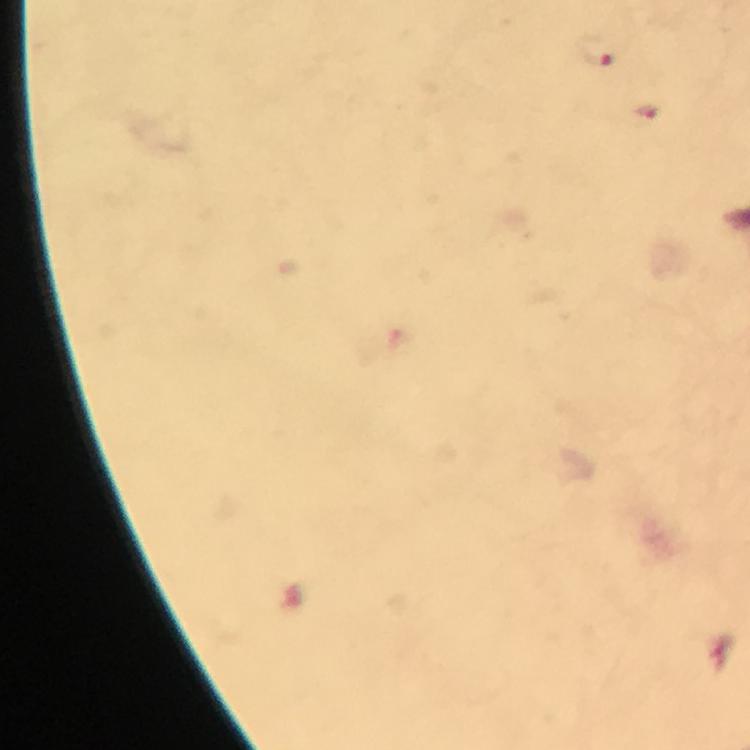

preparation = thick smear
image size = 750×750 pixels
immersion oil = used
capture = smartphone mounted on the microscope
magnification = 100x
context = from a diagnostic examination for malaria
stain = Giemsa
cropped from = one field of view
malaria parasite locations = approximate centers as (x, y) in pixels: (597, 55), (648, 114), (721, 655)